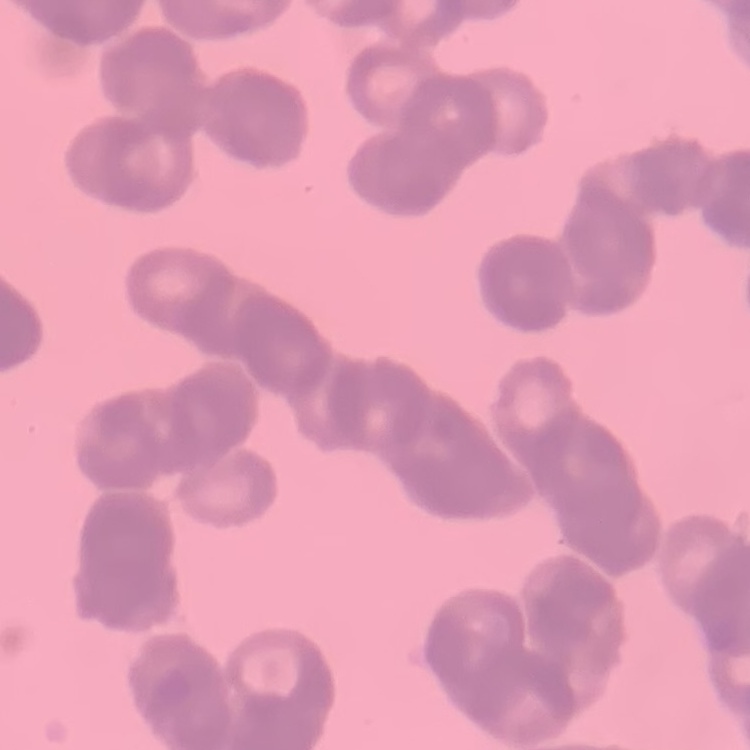

Summary:
  - Red blood cell morphology: rouleaux formation
  - Stain: Field's or Giemsa
  - Image type: square crop of a larger photomicrograph
  - Preparation: thin peripheral smear